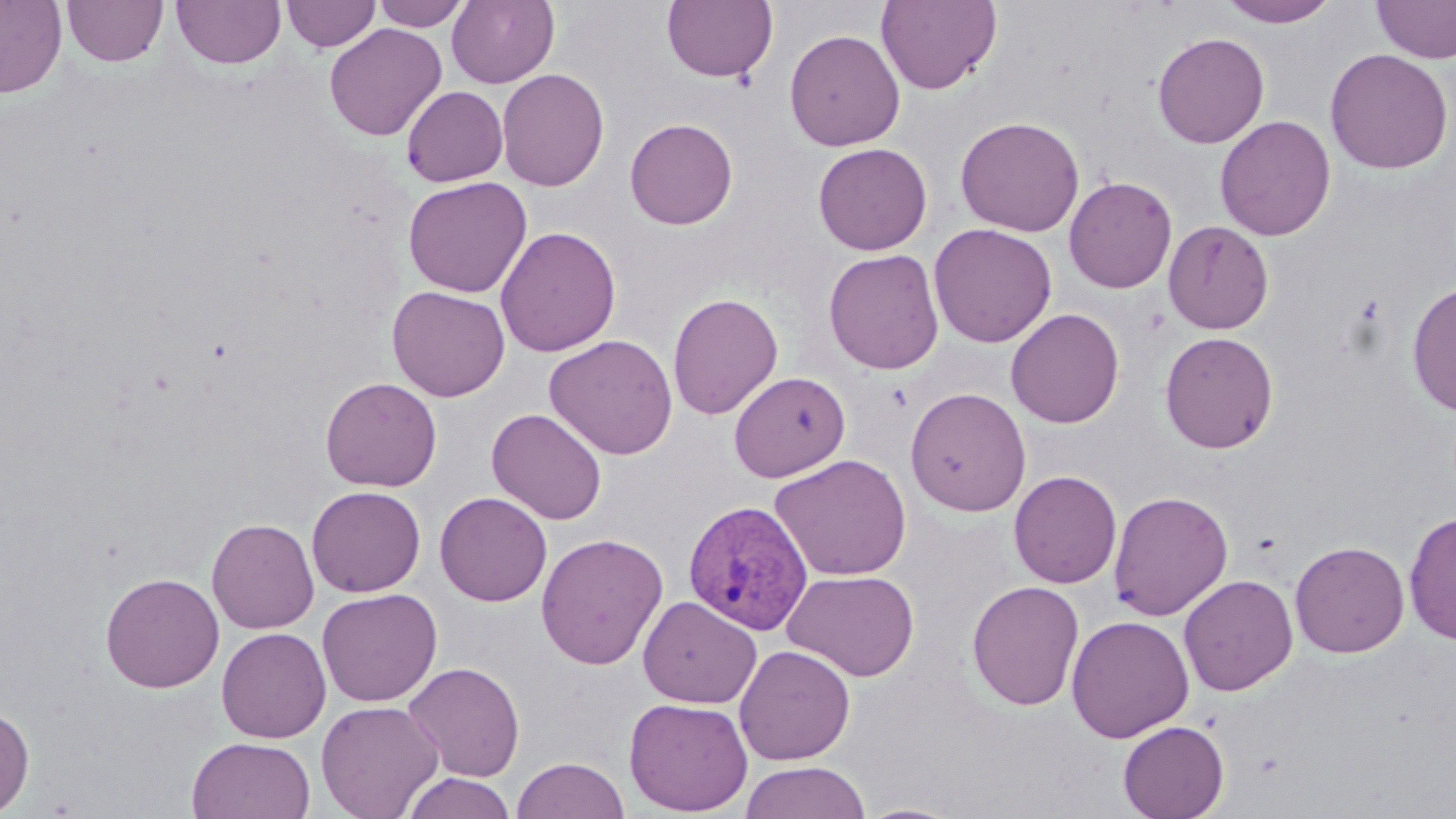
slide_level_diagnosis: Plasmodium vivax
preparation: thin blood smear
magnification: 1000x
plasmodium_vivax_infected_red_blood_cell_locations: 'approximate bounding boxes as named x1/y1/x2/y2 corners in pixels: (x1=683, y1=500, x2=813, y2=636)'
stain: May-Grünwald-Giemsa
image_size: 1456×819 pixels
uninfected_red_blood_cell_locations: 'approximate bounding boxes as named x1/y1/x2/y2 corners in pixels: (x1=0, y1=0, x2=67, y2=98), (x1=62, y1=0, x2=168, y2=67), (x1=171, y1=0, x2=286, y2=69), (x1=281, y1=0, x2=381, y2=52), (x1=372, y1=0, x2=470, y2=31), (x1=447, y1=0, x2=559, y2=88), (x1=661, y1=0, x2=777, y2=82), (x1=875, y1=0, x2=1002, y2=95), (x1=1217, y1=0, x2=1341, y2=27), (x1=1373, y1=0, x2=1456, y2=64), (x1=324, y1=23, x2=447, y2=142), (x1=784, y1=28, x2=906, y2=151), (x1=1152, y1=31, x2=1270, y2=148), (x1=1325, y1=48, x2=1454, y2=174), (x1=496, y1=68, x2=610, y2=191), (x1=401, y1=85, x2=508, y2=187), (x1=955, y1=115, x2=1085, y2=236), (x1=1214, y1=115, x2=1336, y2=241), (x1=625, y1=117, x2=738, y2=229), (x1=813, y1=142, x2=932, y2=255), (x1=403, y1=176, x2=532, y2=297), (x1=1064, y1=176, x2=1177, y2=293), (x1=1163, y1=220, x2=1274, y2=334), (x1=929, y1=223, x2=1057, y2=347), (x1=495, y1=225, x2=621, y2=357), (x1=823, y1=249, x2=945, y2=375), (x1=1407, y1=280, x2=1456, y2=417), (x1=387, y1=285, x2=510, y2=401), (x1=667, y1=292, x2=783, y2=419), (x1=1005, y1=308, x2=1125, y2=428), (x1=1159, y1=331, x2=1279, y2=453), (x1=544, y1=334, x2=678, y2=460), (x1=728, y1=370, x2=850, y2=482), (x1=320, y1=376, x2=442, y2=491), (x1=904, y1=387, x2=1031, y2=517), (x1=487, y1=408, x2=607, y2=524), (x1=770, y1=453, x2=913, y2=581), (x1=1008, y1=470, x2=1122, y2=588), (x1=307, y1=485, x2=426, y2=597), (x1=1107, y1=490, x2=1233, y2=621), (x1=435, y1=491, x2=553, y2=606), (x1=1403, y1=509, x2=1456, y2=646), (x1=206, y1=517, x2=319, y2=633), (x1=535, y1=532, x2=669, y2=671), (x1=1289, y1=540, x2=1410, y2=658), (x1=783, y1=569, x2=920, y2=681), (x1=100, y1=571, x2=224, y2=693), (x1=1179, y1=573, x2=1298, y2=696), (x1=967, y1=580, x2=1085, y2=711), (x1=317, y1=588, x2=442, y2=707), (x1=637, y1=595, x2=762, y2=708), (x1=1066, y1=615, x2=1194, y2=742), (x1=216, y1=627, x2=331, y2=743), (x1=734, y1=644, x2=856, y2=765), (x1=402, y1=661, x2=525, y2=782), (x1=624, y1=697, x2=753, y2=815), (x1=316, y1=700, x2=444, y2=818), (x1=0, y1=701, x2=35, y2=817), (x1=1118, y1=720, x2=1229, y2=819), (x1=187, y1=736, x2=316, y2=819), (x1=512, y1=757, x2=629, y2=818), (x1=740, y1=761, x2=872, y2=819), (x1=400, y1=771, x2=517, y2=819), (x1=855, y1=802, x2=967, y2=819)'
field_of_view: one of a larger specimen
modality: light microscopy